Outline each blood parasite and name the species.
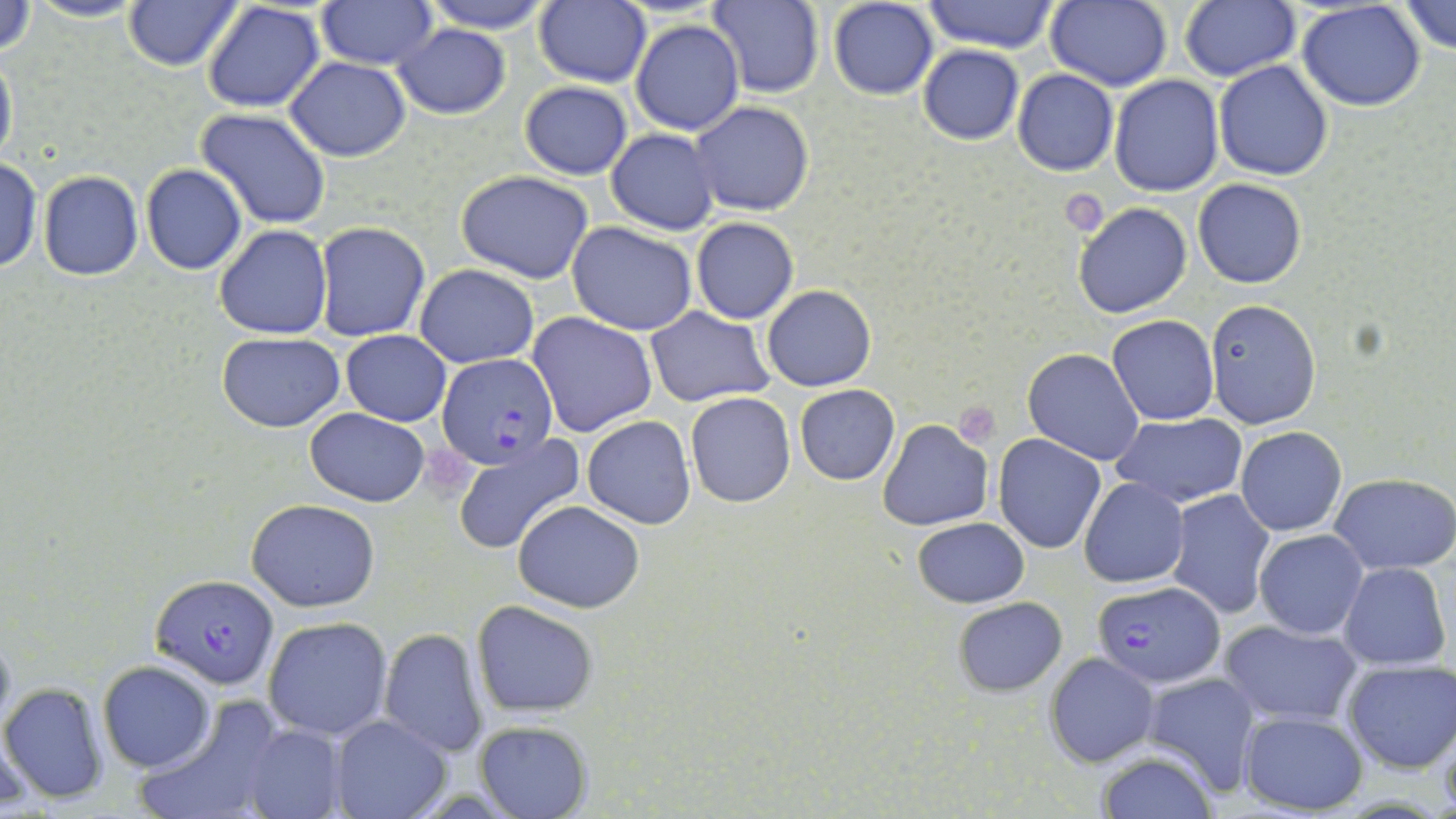

Approximate bounding boxes as named x1/y1/x2/y2 corners in pixels.
Plasmodium falciparum-infected red blood cells: (x1=437, y1=353, x2=559, y2=469), (x1=150, y1=573, x2=279, y2=686), (x1=1091, y1=581, x2=1225, y2=688).
No Plasmodium ovale, Plasmodium malariae, Plasmodium vivax, Babesia divergens, or Trypanosoma brucei observed.

slide_level_diagnosis: Plasmodium falciparum
uninfected_red_blood_cell_locations: 'approximate bounding boxes as named x1/y1/x2/y2 corners in pixels: (x1=0, y1=0, x2=37, y2=61), (x1=23, y1=0, x2=151, y2=24), (x1=123, y1=0, x2=240, y2=71), (x1=419, y1=0, x2=557, y2=34), (x1=534, y1=0, x2=653, y2=89), (x1=710, y1=0, x2=823, y2=99), (x1=827, y1=0, x2=939, y2=100), (x1=923, y1=0, x2=1059, y2=53), (x1=1179, y1=0, x2=1300, y2=83), (x1=1297, y1=0, x2=1426, y2=110), (x1=315, y1=1, x2=438, y2=71), (x1=1043, y1=1, x2=1173, y2=90), (x1=1399, y1=1, x2=1456, y2=55), (x1=201, y1=2, x2=326, y2=113), (x1=629, y1=20, x2=744, y2=136), (x1=391, y1=22, x2=513, y2=120), (x1=916, y1=45, x2=1025, y2=145), (x1=0, y1=46, x2=17, y2=173), (x1=286, y1=56, x2=411, y2=162), (x1=1213, y1=60, x2=1335, y2=181), (x1=1012, y1=69, x2=1119, y2=176), (x1=1108, y1=74, x2=1225, y2=196), (x1=520, y1=81, x2=633, y2=180), (x1=691, y1=101, x2=814, y2=216), (x1=197, y1=108, x2=332, y2=229), (x1=605, y1=127, x2=721, y2=235), (x1=0, y1=157, x2=43, y2=273), (x1=141, y1=164, x2=247, y2=274), (x1=456, y1=171, x2=595, y2=283), (x1=37, y1=172, x2=143, y2=280), (x1=1193, y1=178, x2=1307, y2=288), (x1=1073, y1=201, x2=1193, y2=319), (x1=690, y1=216, x2=799, y2=323), (x1=567, y1=221, x2=698, y2=335), (x1=314, y1=222, x2=430, y2=341), (x1=214, y1=224, x2=333, y2=341), (x1=414, y1=264, x2=540, y2=368), (x1=761, y1=284, x2=876, y2=391), (x1=1204, y1=299, x2=1320, y2=429), (x1=646, y1=306, x2=775, y2=407), (x1=526, y1=312, x2=657, y2=438), (x1=1106, y1=315, x2=1218, y2=424), (x1=340, y1=329, x2=452, y2=425), (x1=217, y1=332, x2=345, y2=431), (x1=1024, y1=348, x2=1145, y2=464), (x1=795, y1=384, x2=901, y2=485), (x1=684, y1=392, x2=796, y2=508), (x1=305, y1=407, x2=431, y2=506), (x1=1114, y1=414, x2=1245, y2=506), (x1=583, y1=415, x2=696, y2=528), (x1=877, y1=419, x2=994, y2=532), (x1=1235, y1=427, x2=1347, y2=535), (x1=451, y1=432, x2=586, y2=554), (x1=993, y1=434, x2=1107, y2=553), (x1=1331, y1=472, x2=1456, y2=574), (x1=1079, y1=477, x2=1188, y2=588), (x1=1167, y1=488, x2=1275, y2=619), (x1=246, y1=498, x2=381, y2=611), (x1=513, y1=500, x2=645, y2=612), (x1=913, y1=516, x2=1029, y2=607), (x1=1255, y1=530, x2=1367, y2=640), (x1=1337, y1=562, x2=1450, y2=670), (x1=953, y1=597, x2=1066, y2=696), (x1=471, y1=600, x2=599, y2=717), (x1=263, y1=616, x2=392, y2=740), (x1=1218, y1=619, x2=1363, y2=727), (x1=379, y1=627, x2=492, y2=757), (x1=1044, y1=652, x2=1158, y2=767), (x1=1341, y1=658, x2=1456, y2=773), (x1=97, y1=661, x2=215, y2=770), (x1=1142, y1=672, x2=1261, y2=795), (x1=1, y1=681, x2=113, y2=803), (x1=132, y1=699, x2=286, y2=819), (x1=1238, y1=710, x2=1369, y2=815), (x1=330, y1=714, x2=451, y2=818), (x1=473, y1=720, x2=592, y2=818), (x1=242, y1=725, x2=345, y2=819), (x1=1096, y1=749, x2=1215, y2=818)'
field_of_view: one of a larger specimen
modality: optical microscopy
stain: May-Grünwald-Giemsa
platelet_locations: 'approximate bounding boxes as named x1/y1/x2/y2 corners in pixels: (x1=952, y1=402, x2=1002, y2=447)'
preparation: thin blood smear
magnification: 1000x
image_size: 1456×819 pixels